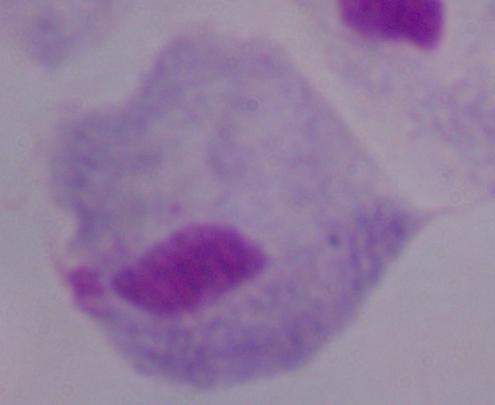
Summary:
  - Magnification: 1000x
  - Modality: micrograph
  - Identification: trichomonad